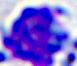

{
  "identification": "leukocyte",
  "modality": "photomicrograph",
  "magnification": "400x"
}